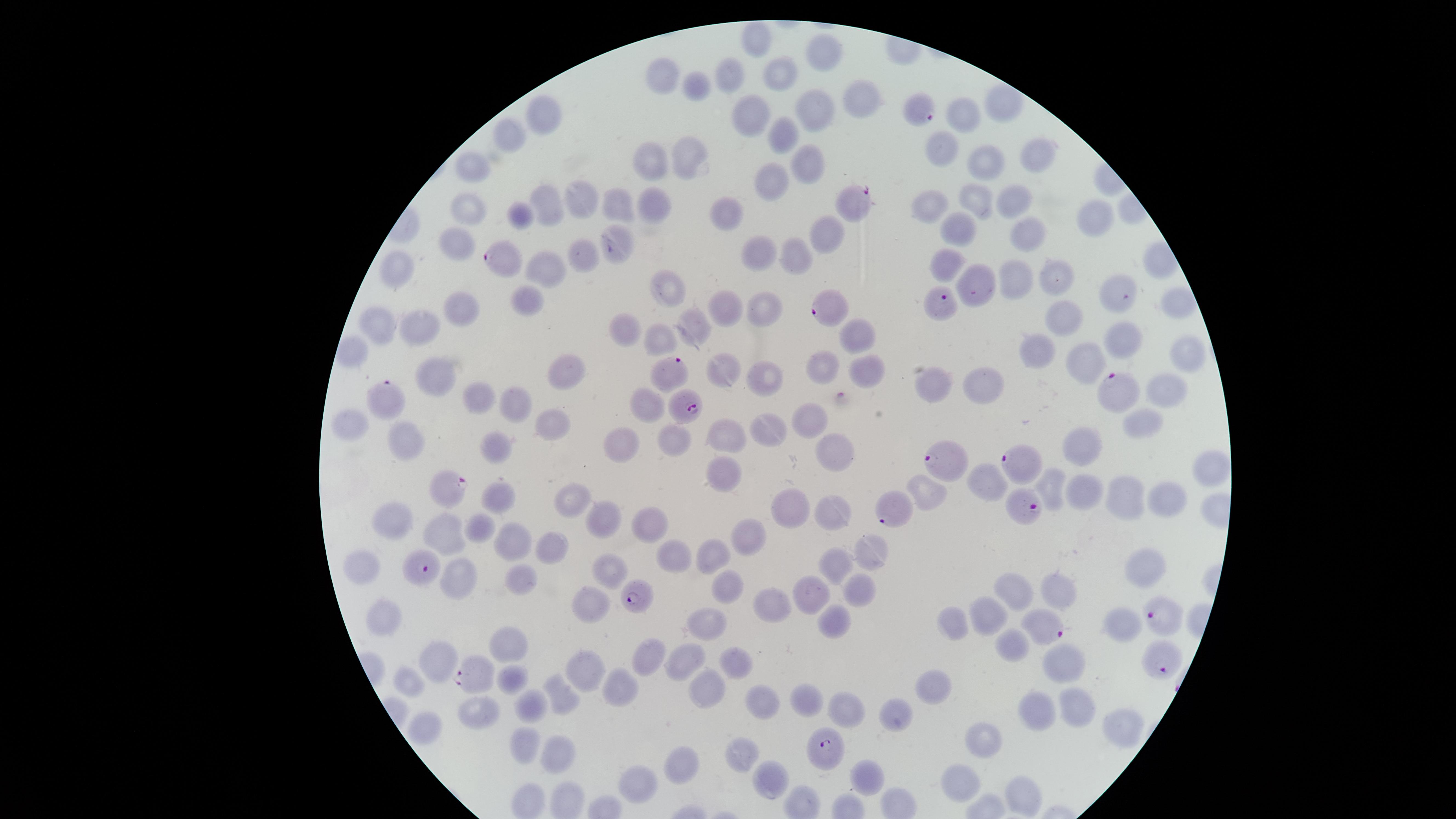
uninfected_RBCs: 'approximate marker points as [x, y] in pixels: [752, 38], [827, 53], [781, 69], [731, 70], [669, 73], [697, 85], [860, 101], [1001, 101], [807, 108], [744, 112], [546, 115], [964, 119], [785, 131], [512, 134], [938, 149], [687, 154], [1033, 154], [652, 159], [806, 159], [982, 160], [478, 170], [774, 177], [579, 197], [1010, 201], [547, 203], [656, 203], [619, 204], [975, 204], [929, 206], [469, 208], [730, 210], [518, 217], [1090, 217], [956, 227], [832, 233], [1023, 234], [455, 240], [621, 247], [755, 252], [796, 254], [577, 257], [947, 265], [403, 270], [545, 270], [1014, 277], [1057, 277], [669, 288], [977, 288], [1120, 289], [527, 302], [1173, 302], [730, 305], [767, 307], [459, 311], [379, 319], [1065, 319], [689, 321], [423, 323], [627, 330], [855, 335], [660, 336], [1127, 338], [1035, 348], [1182, 354], [1080, 364], [731, 371], [862, 371], [815, 372], [562, 375], [435, 376], [767, 381], [985, 384], [932, 386], [1163, 386], [474, 395], [509, 400], [645, 405], [809, 415], [349, 419], [553, 424], [1141, 425], [773, 427], [728, 435], [404, 439], [677, 443], [619, 444], [835, 444], [1082, 445], [498, 448], [1202, 471], [725, 477], [1049, 479], [927, 487], [1088, 491], [499, 493], [1129, 497], [574, 499], [1168, 500], [790, 508], [837, 510], [403, 514], [602, 516], [480, 523], [646, 525], [448, 534], [511, 537], [747, 540], [552, 545], [872, 553], [672, 554], [714, 555], [839, 565], [371, 566], [610, 566], [1143, 566], [457, 577], [519, 584], [722, 585], [857, 588], [1060, 591], [813, 593], [1017, 593], [779, 600], [590, 601], [991, 616], [385, 620], [833, 620], [1121, 624], [707, 625], [953, 627], [1007, 640], [514, 649], [646, 658], [685, 660], [1067, 661], [440, 662], [735, 662], [591, 666], [410, 680], [513, 681], [931, 681], [622, 685], [709, 685], [565, 693], [809, 696], [756, 703], [845, 703], [539, 704], [1044, 708], [484, 712], [1076, 712], [899, 714], [1124, 723], [422, 727], [987, 738], [522, 746], [742, 750], [560, 755], [685, 761], [871, 775], [641, 778], [961, 779], [769, 782], [1024, 794]'
visible_region: circular
presence: malaria parasites detected
parasitized_RBCs: 'approximate marker points as [x, y] in pixels: [919, 107], [850, 203], [499, 257], [940, 305], [826, 311], [675, 372], [1118, 383], [389, 399], [684, 401], [1022, 460], [946, 461], [450, 486], [1025, 501], [898, 509], [422, 570], [640, 597], [1157, 614], [1045, 629], [1158, 664], [470, 675], [827, 750]'
image_size: 1456×819 pixels
stain: Giemsa
capture: smartphone photograph through the microscope eyepiece
field_of_view: single
preparation: thin blood film
species: Plasmodium falciparum